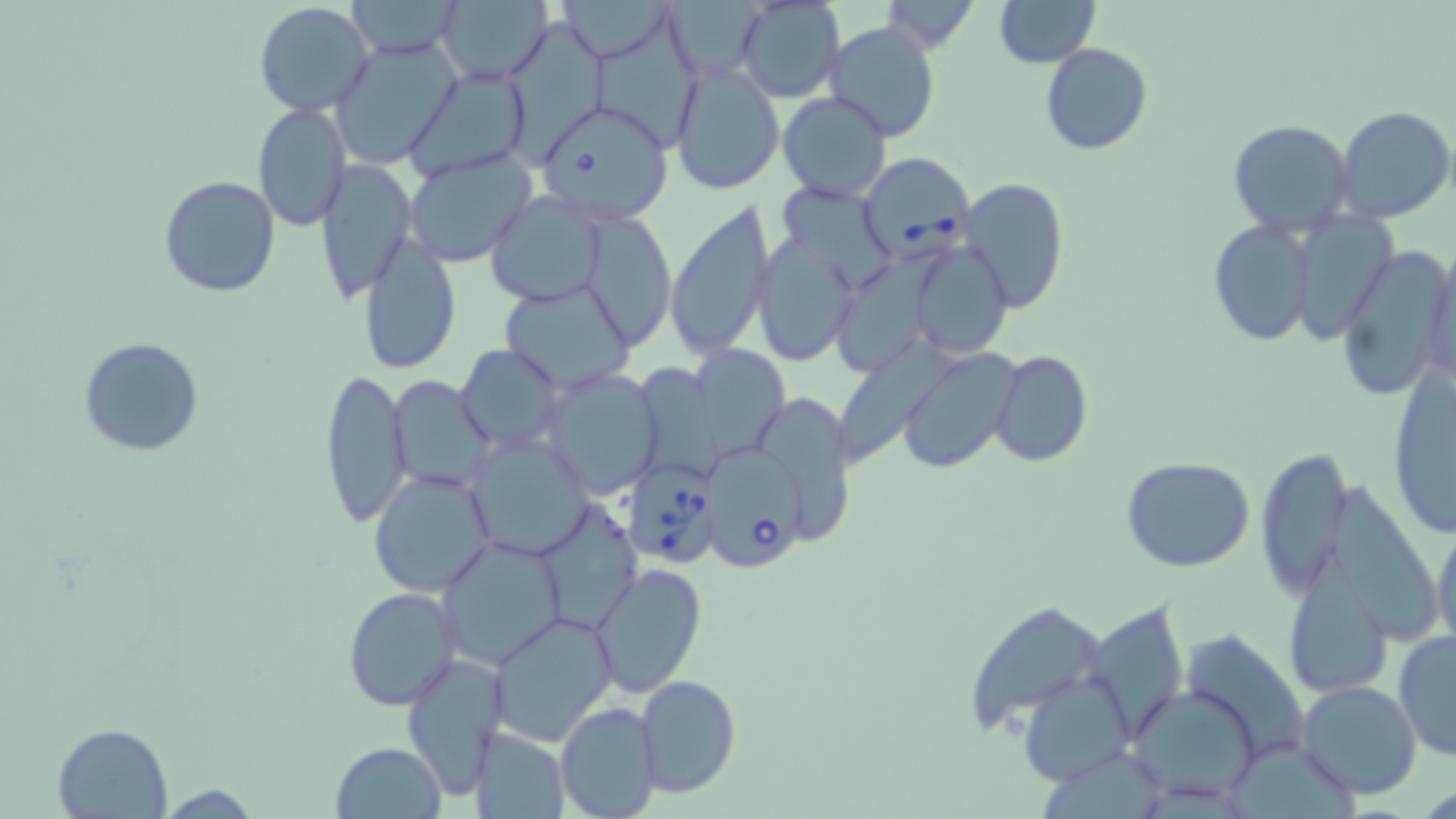
Summary:
  - Coordinate format: approximate bounding boxes as named x1/y1/x2/y2 corners in pixels
  - Babesia divergens-infected red blood cell locations: (x1=855, y1=153, x2=976, y2=263), (x1=703, y1=448, x2=810, y2=570), (x1=624, y1=461, x2=718, y2=567)
  - Uninfected red blood cell locations: (x1=345, y1=0, x2=467, y2=59), (x1=554, y1=0, x2=675, y2=63), (x1=733, y1=0, x2=846, y2=103), (x1=877, y1=0, x2=984, y2=52), (x1=994, y1=0, x2=1101, y2=67), (x1=253, y1=1, x2=375, y2=117), (x1=436, y1=1, x2=554, y2=84), (x1=589, y1=20, x2=702, y2=150), (x1=824, y1=21, x2=942, y2=145), (x1=504, y1=31, x2=605, y2=169), (x1=332, y1=40, x2=460, y2=169), (x1=1041, y1=43, x2=1151, y2=155), (x1=669, y1=60, x2=785, y2=195), (x1=405, y1=67, x2=531, y2=179), (x1=777, y1=91, x2=892, y2=203), (x1=253, y1=102, x2=350, y2=230), (x1=538, y1=103, x2=672, y2=223), (x1=1334, y1=104, x2=1454, y2=224), (x1=1229, y1=120, x2=1356, y2=236), (x1=403, y1=149, x2=537, y2=268), (x1=314, y1=160, x2=414, y2=302), (x1=158, y1=175, x2=280, y2=297), (x1=957, y1=177, x2=1071, y2=314), (x1=781, y1=182, x2=900, y2=289), (x1=484, y1=191, x2=608, y2=307), (x1=663, y1=198, x2=776, y2=363), (x1=1285, y1=210, x2=1398, y2=345), (x1=587, y1=213, x2=672, y2=343), (x1=1207, y1=218, x2=1320, y2=348), (x1=755, y1=232, x2=861, y2=369), (x1=357, y1=234, x2=460, y2=374), (x1=911, y1=238, x2=1011, y2=360), (x1=1420, y1=242, x2=1456, y2=396), (x1=834, y1=244, x2=951, y2=367), (x1=1336, y1=245, x2=1453, y2=405), (x1=500, y1=281, x2=636, y2=394), (x1=842, y1=332, x2=959, y2=460), (x1=78, y1=337, x2=205, y2=457), (x1=688, y1=340, x2=792, y2=458), (x1=457, y1=344, x2=564, y2=452), (x1=897, y1=347, x2=1023, y2=474), (x1=990, y1=350, x2=1093, y2=469), (x1=637, y1=361, x2=727, y2=485), (x1=1387, y1=362, x2=1454, y2=543), (x1=318, y1=367, x2=413, y2=530), (x1=542, y1=369, x2=665, y2=497), (x1=389, y1=375, x2=497, y2=493), (x1=762, y1=392, x2=855, y2=543), (x1=464, y1=433, x2=592, y2=561), (x1=1253, y1=446, x2=1350, y2=596), (x1=1120, y1=456, x2=1255, y2=572), (x1=368, y1=468, x2=495, y2=597), (x1=1333, y1=475, x2=1441, y2=650), (x1=535, y1=500, x2=640, y2=635), (x1=1432, y1=515, x2=1455, y2=655), (x1=435, y1=535, x2=564, y2=670), (x1=1282, y1=548, x2=1393, y2=697), (x1=590, y1=564, x2=707, y2=700), (x1=341, y1=587, x2=461, y2=709), (x1=963, y1=600, x2=1107, y2=735), (x1=1084, y1=601, x2=1188, y2=744), (x1=490, y1=611, x2=617, y2=747), (x1=1180, y1=629, x2=1311, y2=768), (x1=1393, y1=630, x2=1456, y2=760), (x1=402, y1=653, x2=509, y2=801), (x1=1022, y1=668, x2=1135, y2=786), (x1=636, y1=674, x2=742, y2=798), (x1=1297, y1=679, x2=1423, y2=801), (x1=1127, y1=683, x2=1262, y2=805), (x1=555, y1=702, x2=662, y2=819), (x1=52, y1=723, x2=174, y2=817), (x1=468, y1=727, x2=570, y2=819), (x1=331, y1=741, x2=448, y2=818)
  - Slide-level diagnosis: Babesia divergens
  - Field of view: one of a larger specimen
  - Image size: 1456×819 pixels
  - Modality: optical microscopy
  - Stain: May-Grünwald-Giemsa
  - Magnification: 1000x
  - Preparation: thin blood film